Report the malaria status of this cell.
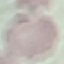
Uninfected.

Acquired by smartphone through the microscope eyepiece. Thin smear of blood. Giemsa stain. Cell patch, automatically extracted from a larger field of view and resized to 64 × 64 pixels.